Identify the parasite.
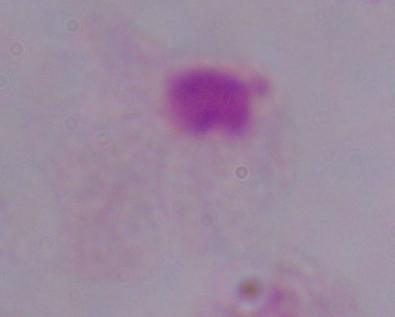
This is a trichomonad.

Micrograph. 1000x magnification.